Describe the morphology of the red blood cells.
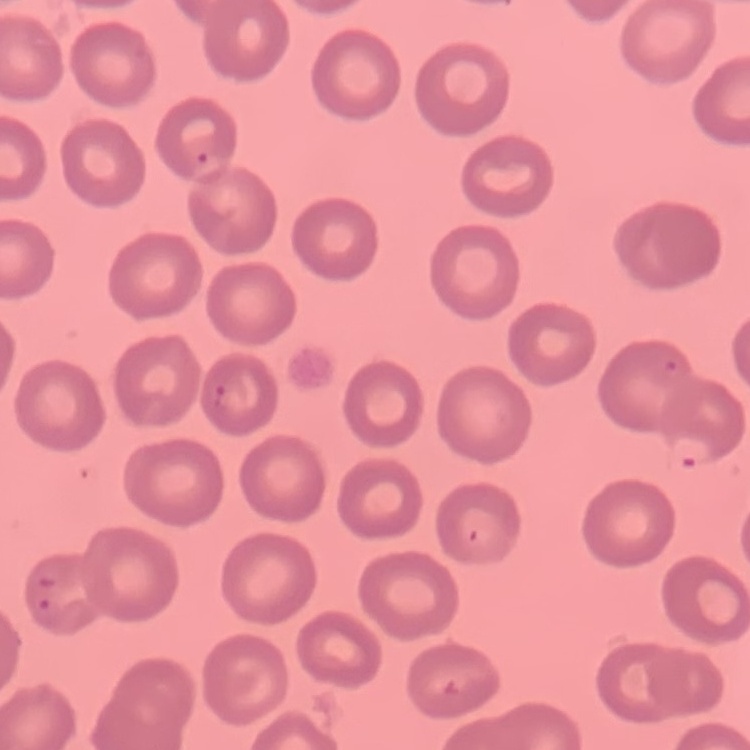
No rouleaux formation.

image type = square crop of a larger photomicrograph
stain = Field's or Giemsa
preparation = thin blood film